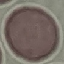

Summary:
  - Malaria status: uninfected
  - Stain: Giemsa
  - Preparation: thin smear
  - Image type: automatically extracted cell patch, resized to 64 × 64 pixels
  - Capture: smartphone camera at the microscope eyepiece